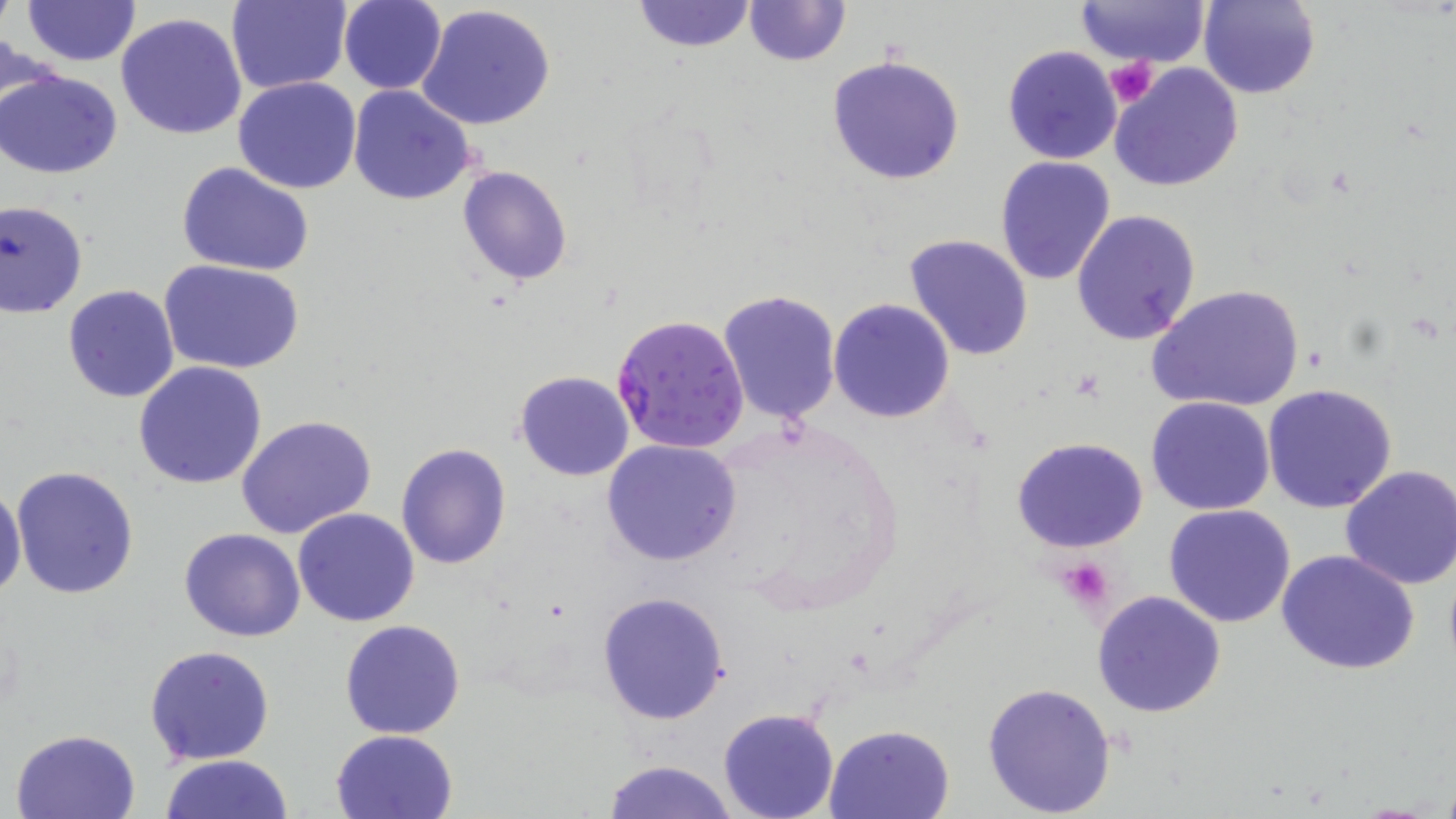 Approximate bounding boxes as [x1, y1, x2, y2] in pixels. Plasmodium falciparum-infected red blood cell locations: [611, 314, 750, 455]. Platelet locations: [1107, 57, 1160, 108], [1057, 557, 1117, 612]. Uninfected red blood cell locations: [226, 0, 351, 95], [630, 0, 758, 51], [1076, 0, 1211, 66], [1200, 0, 1321, 100], [21, 1, 141, 66], [338, 1, 446, 93], [742, 1, 851, 67], [417, 5, 558, 131], [115, 12, 248, 141], [1002, 45, 1123, 165], [826, 55, 965, 185], [1109, 62, 1244, 193], [1, 68, 123, 178], [234, 77, 362, 193], [347, 85, 477, 204], [994, 155, 1117, 288], [176, 162, 316, 276], [458, 165, 573, 285], [1, 200, 88, 317], [1071, 209, 1201, 345], [905, 235, 1033, 361], [159, 260, 303, 374], [1146, 283, 1306, 416], [63, 284, 179, 403], [717, 290, 842, 425], [828, 298, 956, 423], [135, 361, 267, 487], [515, 370, 634, 481], [1261, 383, 1398, 513], [1146, 395, 1276, 515], [237, 416, 376, 539], [1012, 435, 1149, 553], [601, 439, 742, 565], [396, 443, 512, 570], [10, 464, 140, 600], [1336, 464, 1455, 590], [0, 485, 26, 602], [1164, 504, 1297, 627], [293, 508, 421, 628], [179, 527, 306, 642], [1276, 549, 1421, 674], [1090, 590, 1227, 718], [596, 591, 730, 724], [339, 619, 467, 739], [144, 644, 275, 767], [980, 680, 1117, 816], [718, 708, 838, 819], [824, 723, 954, 818], [12, 727, 141, 819], [330, 729, 459, 819], [160, 754, 294, 819], [601, 759, 739, 819]. Slide-level diagnosis: Plasmodium falciparum. Image is 1456×819 pixels. Single field of view. May-Grünwald-Giemsa-stained preparation. Captured at 1000x magnification. Thin blood film. Light microscopy.